Assess this cell for malaria.
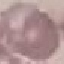
It is uninfected.

Automatically extracted cell patch, resized to 64 × 64 pixels. Thin blood film. Acquired by smartphone through the microscope eyepiece. Giemsa-stained preparation.